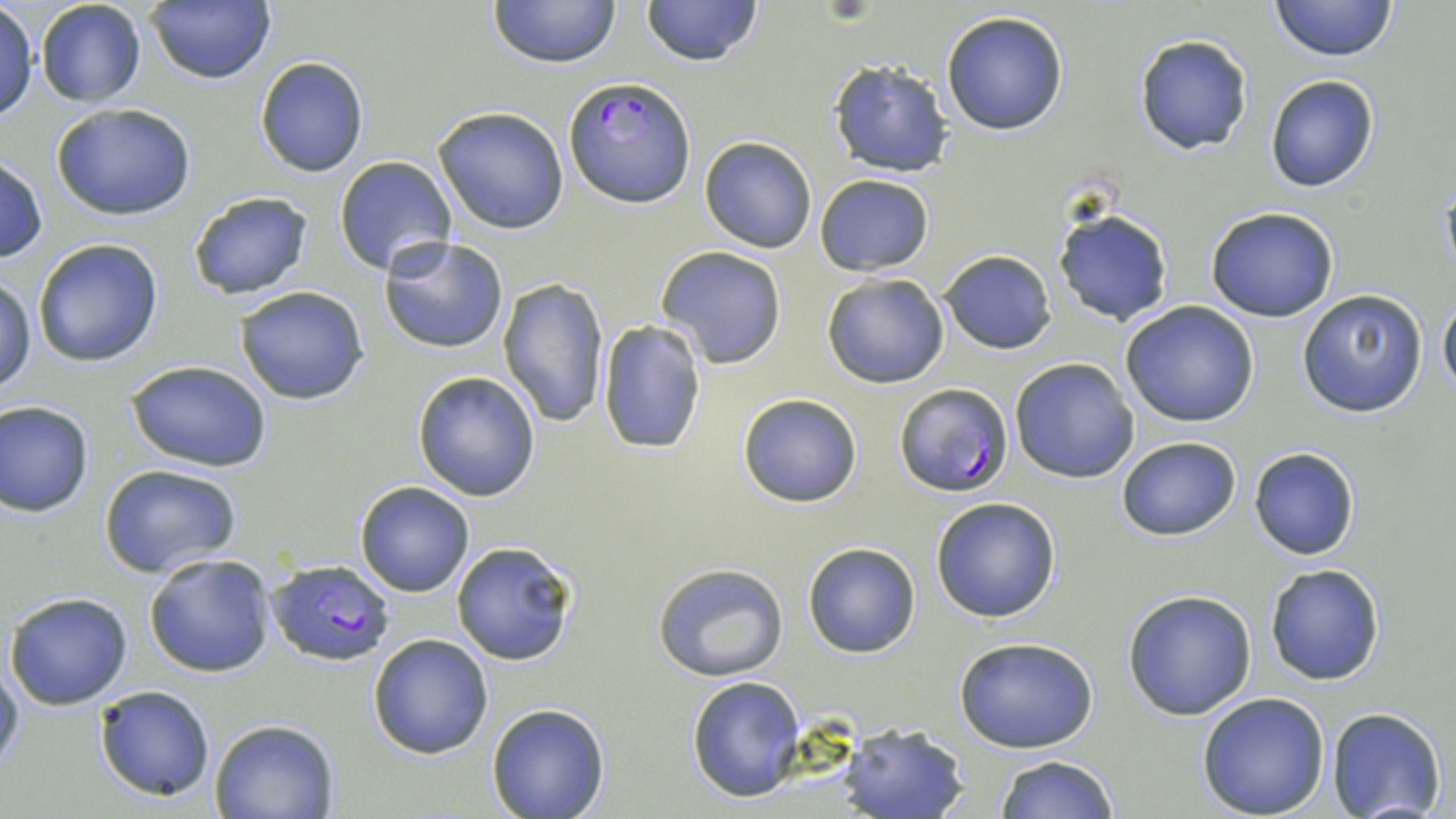

Approximate bounding boxes as (x1,y1)-(x2,y2) corner pairs in pixels. Uninfected red blood cell locations: (147,0)-(275,84), (488,0)-(621,69), (640,0)-(763,68), (1269,0)-(1398,61), (35,1)-(149,107), (1,4)-(38,123), (941,10)-(1070,135), (1134,33)-(1253,156), (254,57)-(369,177), (827,59)-(954,177), (1264,75)-(1380,192), (52,102)-(197,221), (433,106)-(569,233), (700,135)-(817,253), (0,153)-(47,264), (334,156)-(458,275), (815,174)-(934,275), (186,190)-(314,301), (1052,206)-(1173,326), (1205,206)-(1340,321), (379,236)-(509,354), (32,238)-(163,368), (656,246)-(787,369), (940,249)-(1057,354), (1,273)-(36,396), (822,273)-(949,388), (496,277)-(609,426), (235,286)-(370,404), (1296,288)-(1428,418), (1439,293)-(1456,394), (1119,301)-(1261,426), (597,319)-(707,455), (1010,358)-(1140,483), (126,360)-(271,472), (412,371)-(542,501), (737,392)-(864,507), (0,399)-(96,517), (1117,435)-(1240,541), (1249,447)-(1360,560), (97,464)-(244,579), (354,481)-(475,597), (931,496)-(1061,622), (450,541)-(579,666), (802,541)-(922,659), (143,552)-(277,678), (651,563)-(789,681), (1264,565)-(1384,685), (1122,589)-(1259,720), (4,591)-(134,711), (368,633)-(494,758), (954,638)-(1099,753), (0,658)-(24,777), (687,675)-(806,802), (92,684)-(218,803), (1195,691)-(1331,818), (487,704)-(610,819), (1326,708)-(1447,819), (209,719)-(338,819), (834,719)-(971,819), (994,755)-(1120,819). Plasmodium falciparum-infected red blood cell locations: (564,76)-(696,207), (893,385)-(1012,497), (266,561)-(395,666). Slide-level diagnosis: Plasmodium falciparum. Thin blood smear. May-Grünwald-Giemsa-stained preparation. Single field of view. Image is 1456×819 pixels. Captured at 1000x magnification. Light microscopy.